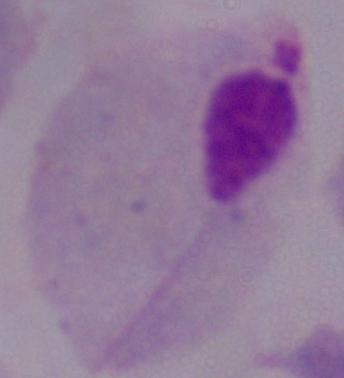

identification = trichomonad
modality = micrograph
magnification = 1000x